Name the cell type shown.
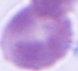

This is an erythrocyte.

Micrograph. Captured at 1000x magnification.